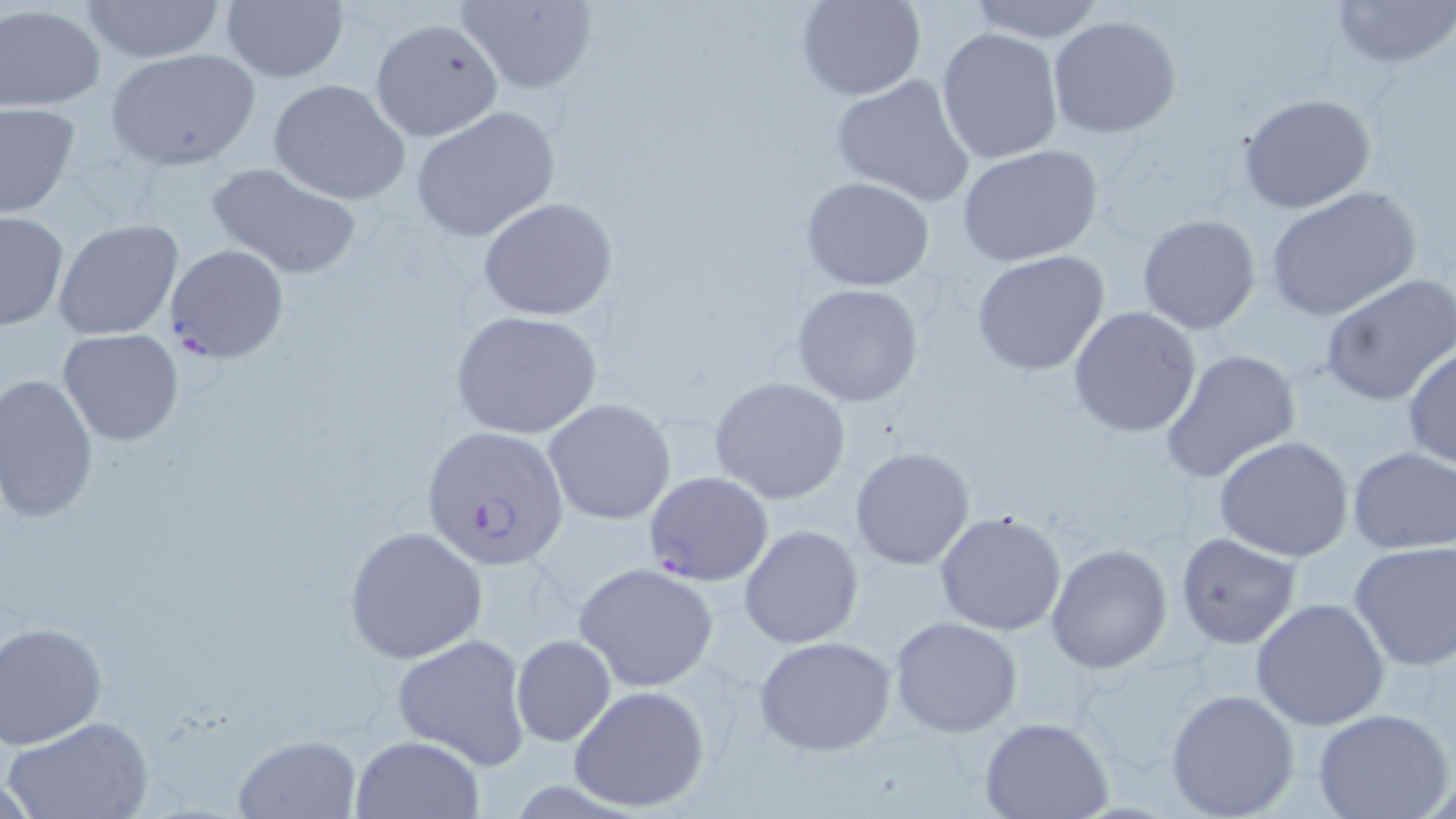
slide-level diagnosis = Plasmodium falciparum
image size = 1456×819 pixels
uninfected red blood cell locations = approximate bounding boxes as (x1,y1)-(x2,y2) corner pairs in pixels: (79,0)-(226,64), (221,0)-(347,83), (795,0)-(926,100), (966,0)-(1107,42), (1330,0)-(1455,71), (455,1)-(597,92), (0,3)-(104,111), (1047,15)-(1182,139), (369,18)-(504,142), (936,28)-(1063,164), (105,47)-(261,170), (831,73)-(977,208), (267,79)-(411,204), (1237,93)-(1378,214), (0,102)-(80,218), (410,106)-(560,242), (956,144)-(1104,268), (204,162)-(363,279), (801,175)-(936,292), (1265,186)-(1422,324), (477,196)-(620,322), (0,211)-(69,332), (1135,214)-(1262,335), (52,219)-(184,339), (971,250)-(1113,377), (1319,274)-(1456,408), (792,282)-(927,408), (1068,305)-(1203,437), (450,310)-(603,439), (58,329)-(185,445), (1402,345)-(1455,471), (1161,349)-(1300,484), (0,373)-(100,523), (708,376)-(851,504), (543,398)-(676,525), (1213,435)-(1355,561), (850,446)-(976,570), (1347,446)-(1456,555), (934,510)-(1068,637), (738,523)-(864,650), (344,525)-(488,664), (1173,530)-(1303,650), (1348,540)-(1456,671), (1045,544)-(1172,674), (573,562)-(720,692), (1249,596)-(1391,731), (889,616)-(1023,737), (0,621)-(108,749), (391,632)-(531,769), (510,633)-(617,748), (753,635)-(898,757), (570,684)-(711,812), (1164,687)-(1301,818), (1312,709)-(1454,819), (6,715)-(155,819), (978,716)-(1115,819), (231,733)-(362,818), (350,735)-(486,819)
field of view = one of a larger specimen
Plasmodium falciparum-infected red blood cell locations = approximate bounding boxes as (x1,y1)-(x2,y2) corner pairs in pixels: (164,244)-(290,364), (424,426)-(568,568), (645,471)-(774,587)
stain = May-Grünwald-Giemsa
modality = light microscopy
preparation = thin blood smear
magnification = 1000x